Report the malaria status of this cell.
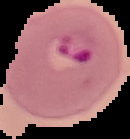

It is parasitized.

image_size: 130×139 pixels
image_type: segmented cell region with the area outside set to black
preparation: thin blood smear